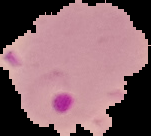
malaria_status: parasitized
image_size: 151×136 pixels
image_type: segmented cell region with the area outside set to black
preparation: thin blood smear